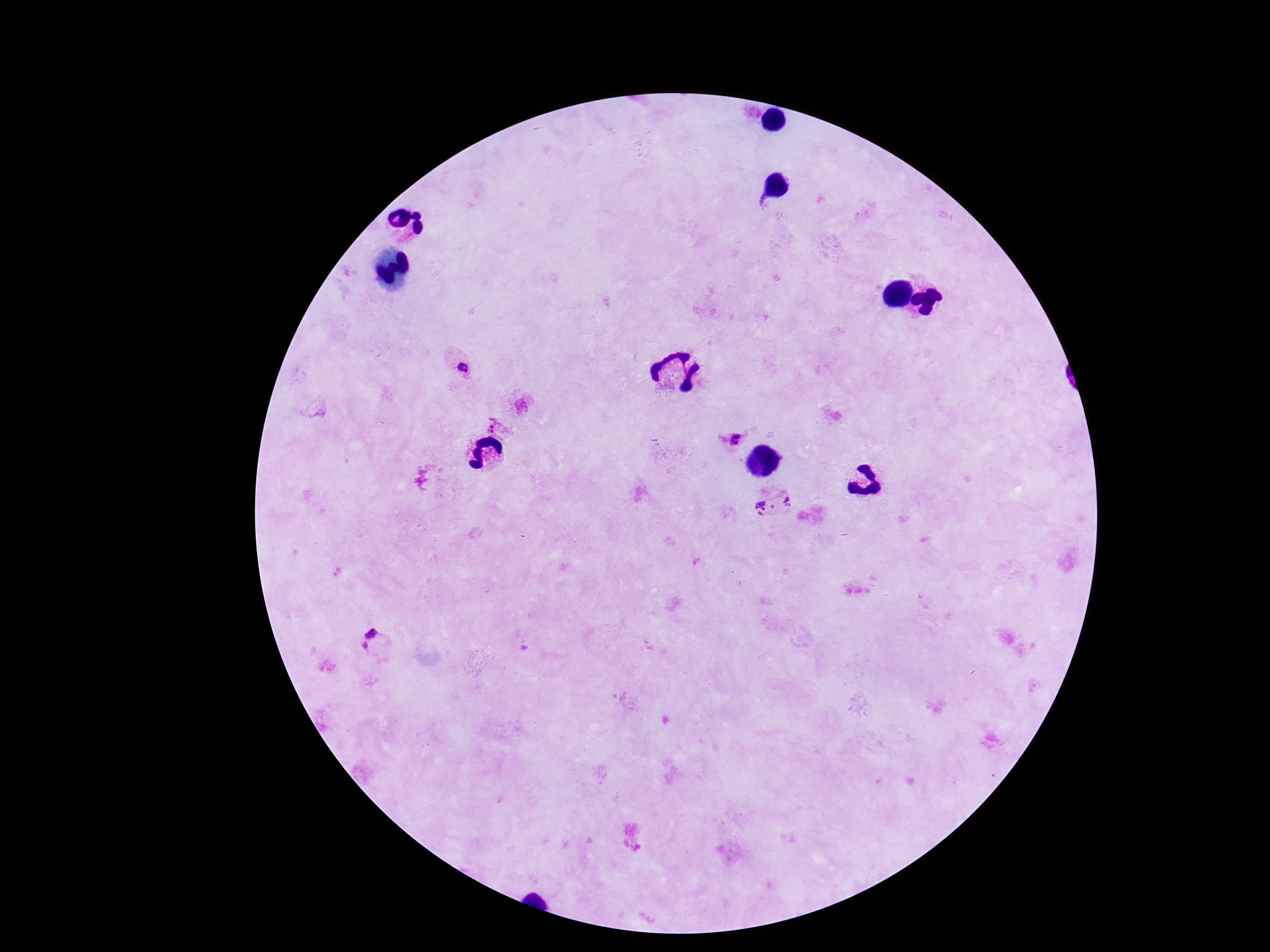

patient malaria status = positive
field of view = one from this slide
capture = smartphone camera through the microscope eyepiece
preparation = thick blood smear
image size = 1270×952 pixels
Plasmodium parasite locations = approximate object centers, in pixels from the top-left corner: (x=464, y=369), (x=495, y=424), (x=733, y=439), (x=775, y=505), (x=372, y=639)
magnification = 100x
stain = Giemsa